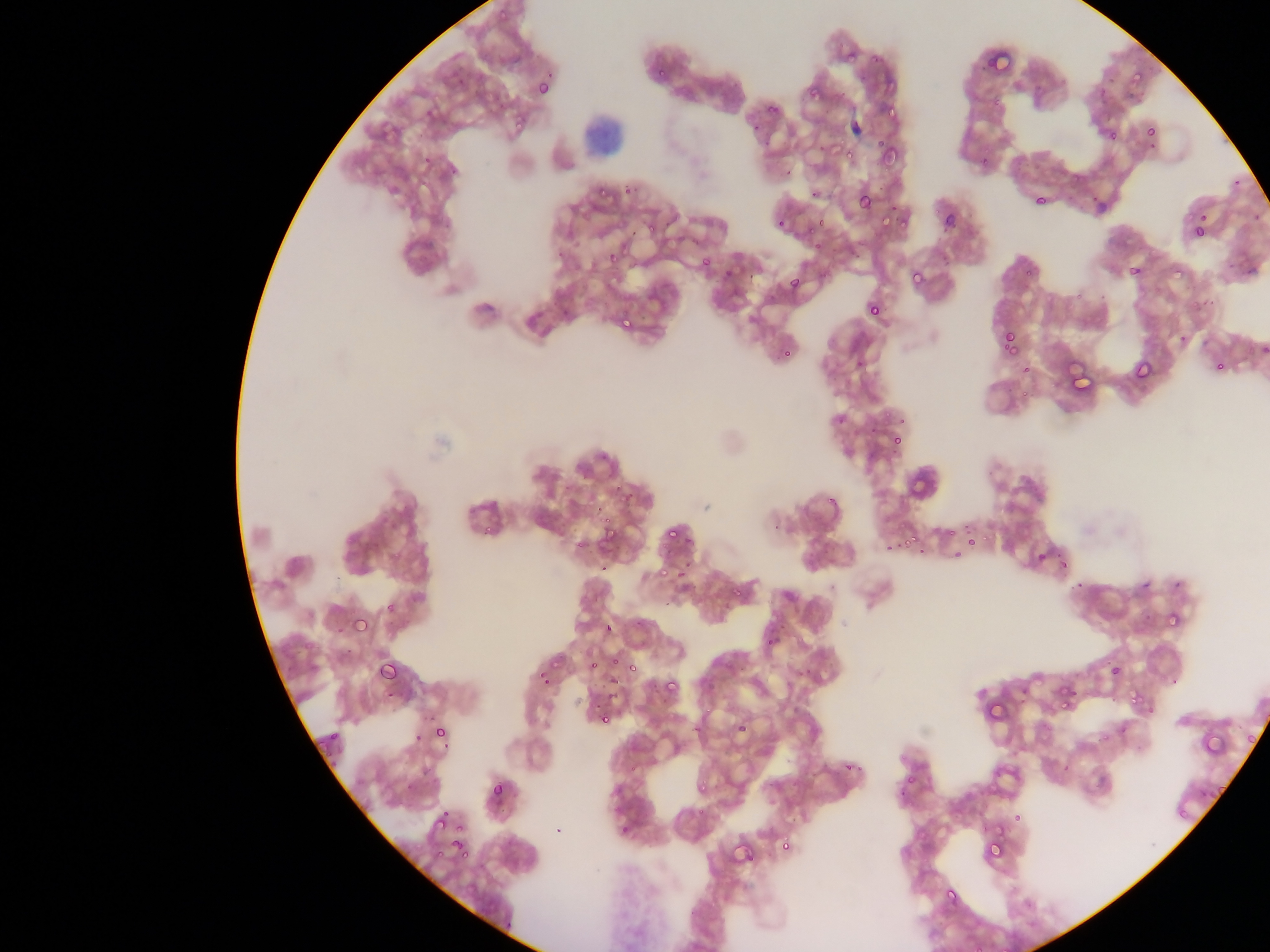
field of view = single
country = Ghana
image size = 1270×952 pixels
Plasmodium parasite locations = approximate bounding boxes as (left, top, right, bottom) in pixels (subset; some below the resolvable size): (488, 11, 516, 27), (841, 42, 867, 66), (982, 45, 1018, 82), (1095, 59, 1124, 98), (1129, 62, 1155, 81), (650, 65, 668, 84), (872, 77, 900, 94), (536, 78, 556, 100), (807, 83, 832, 111), (765, 92, 783, 113), (875, 106, 897, 123), (511, 111, 532, 135), (1144, 124, 1160, 140), (875, 140, 903, 169), (844, 145, 859, 160), (821, 149, 843, 164), (421, 153, 436, 169), (591, 185, 611, 201), (856, 191, 876, 212), (1033, 194, 1049, 209), (939, 211, 958, 233), (774, 214, 791, 233), (874, 215, 896, 228), (1193, 225, 1209, 242), (555, 249, 567, 261), (605, 254, 620, 266), (697, 255, 714, 274), (1127, 264, 1145, 283), (721, 265, 736, 282), (1173, 265, 1186, 281), (906, 268, 926, 291), (786, 273, 806, 294), (865, 300, 885, 321), (622, 311, 637, 328), (998, 327, 1026, 360), (1002, 332, 1020, 353), (1172, 335, 1188, 350), (779, 346, 796, 364), (1131, 359, 1154, 385), (1209, 362, 1231, 371), (1063, 372, 1098, 396), (889, 431, 906, 451), (597, 519, 622, 549), (662, 525, 681, 545), (893, 528, 923, 553), (1032, 546, 1058, 573), (1033, 549, 1050, 566), (1057, 557, 1071, 573), (673, 562, 693, 585), (654, 569, 669, 577), (383, 595, 400, 615), (351, 614, 372, 638), (1156, 619, 1182, 626), (601, 620, 617, 637), (377, 656, 405, 685), (627, 658, 645, 674), (588, 661, 604, 670), (533, 662, 556, 680), (1108, 662, 1124, 680), (659, 676, 682, 701), (1057, 687, 1081, 714), (1127, 688, 1146, 709), (983, 699, 1007, 725), (594, 709, 614, 729), (1246, 718, 1256, 748), (1196, 721, 1236, 758), (431, 724, 452, 747), (1210, 767, 1233, 798), (488, 779, 511, 805), (430, 818, 448, 833), (983, 835, 1007, 863), (776, 841, 796, 855), (448, 842, 466, 855), (935, 887, 961, 911)
capture = mobile-phone photograph through a microscope
preparation = thin blood film